Describe the morphology of the erythrocytes.
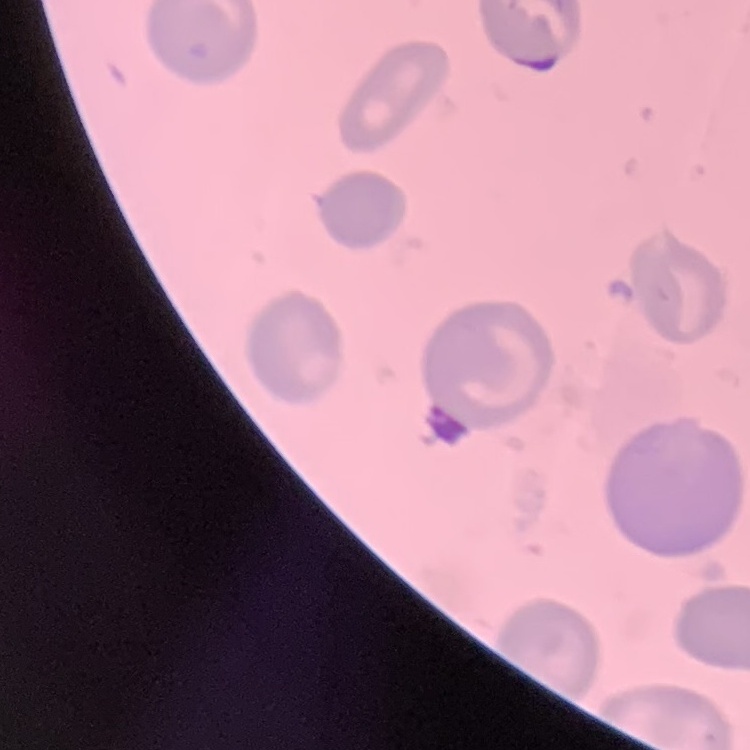

No rouleaux formation.

Summary:
  - Preparation: thin blood smear
  - Stain: Field's or Giemsa
  - Image type: square crop of a larger photomicrograph